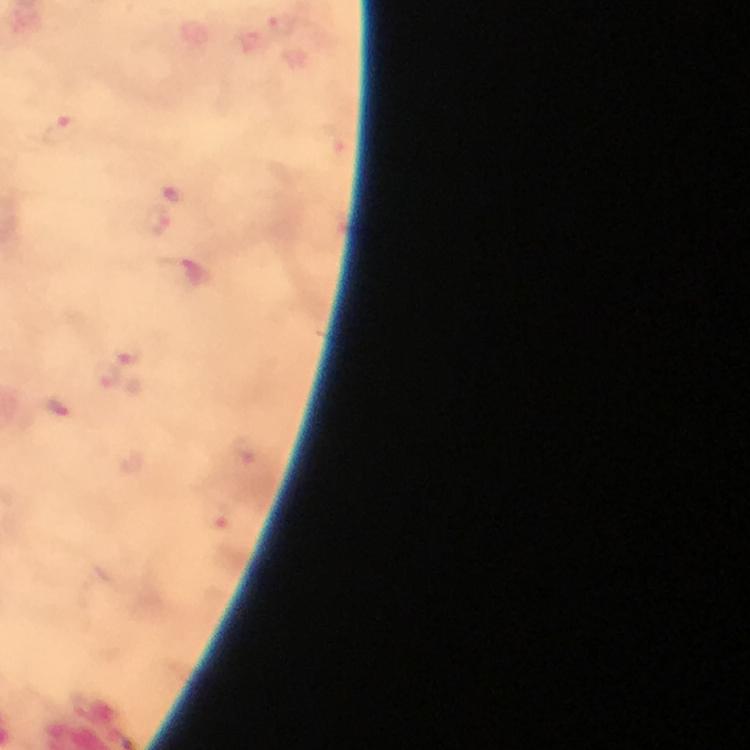
Approximate object centers, in pixels from the top-left corner.
Summary:
  - Malaria parasite locations: (x=281, y=24), (x=61, y=130), (x=154, y=222), (x=131, y=352), (x=107, y=374), (x=245, y=451), (x=217, y=519)
  - Cropped from: one field of view
  - Capture: smartphone photograph through a microscope
  - Magnification: 100x
  - Image size: 750×750 pixels
  - Immersion oil: used
  - Preparation: thick blood smear
  - Stain: Giemsa
  - Context: from a diagnostic examination for malaria